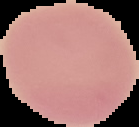
image type = segmented cell region on a black background
result = no malaria parasites seen
image size = 139×127 pixels
preparation = thin blood film